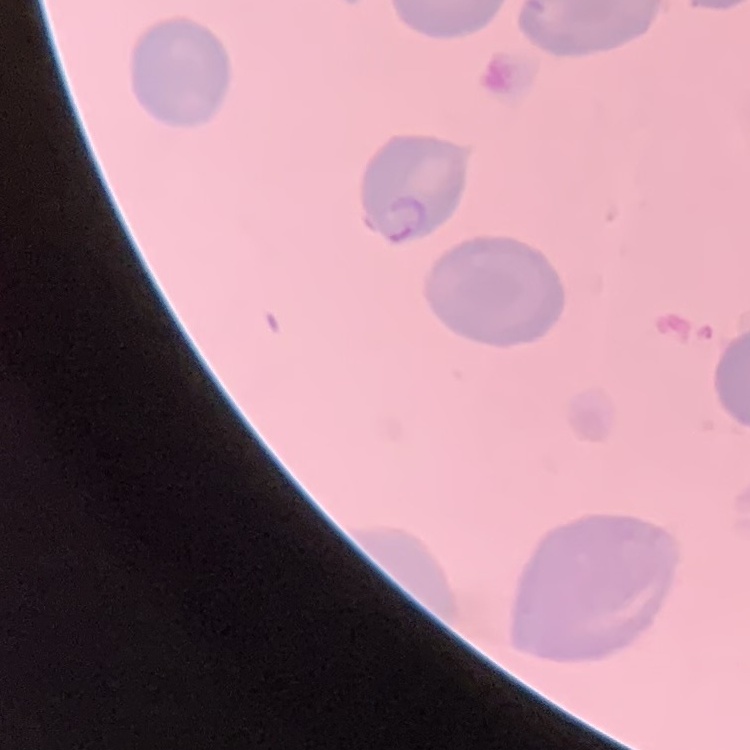 The red blood cells show no rouleaux formation. One tile cut from a larger photomicrograph. Thin peripheral smear. Field's or Giemsa stain.